Describe the morphology of the red blood cells.
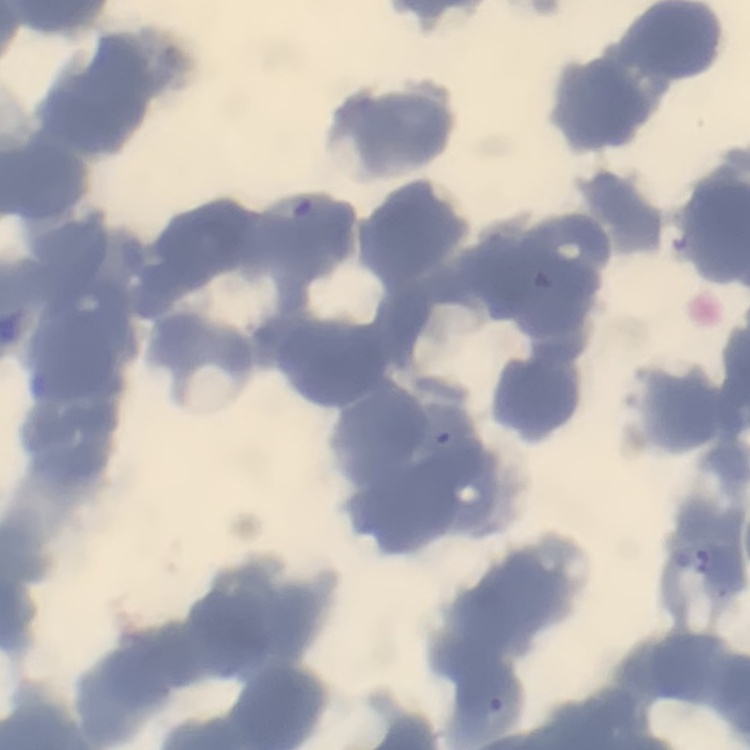

Rouleaux formation.

Stained with either Field's or Giemsa. Square crop of a larger photomicrograph. Thin blood smear.